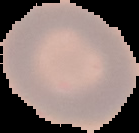

malaria status = uninfected
image size = 139×133 pixels
image type = cell region segmented out of the field of view; surrounding area masked to black
preparation = thin blood film